Locate every uninfected red blood cell.
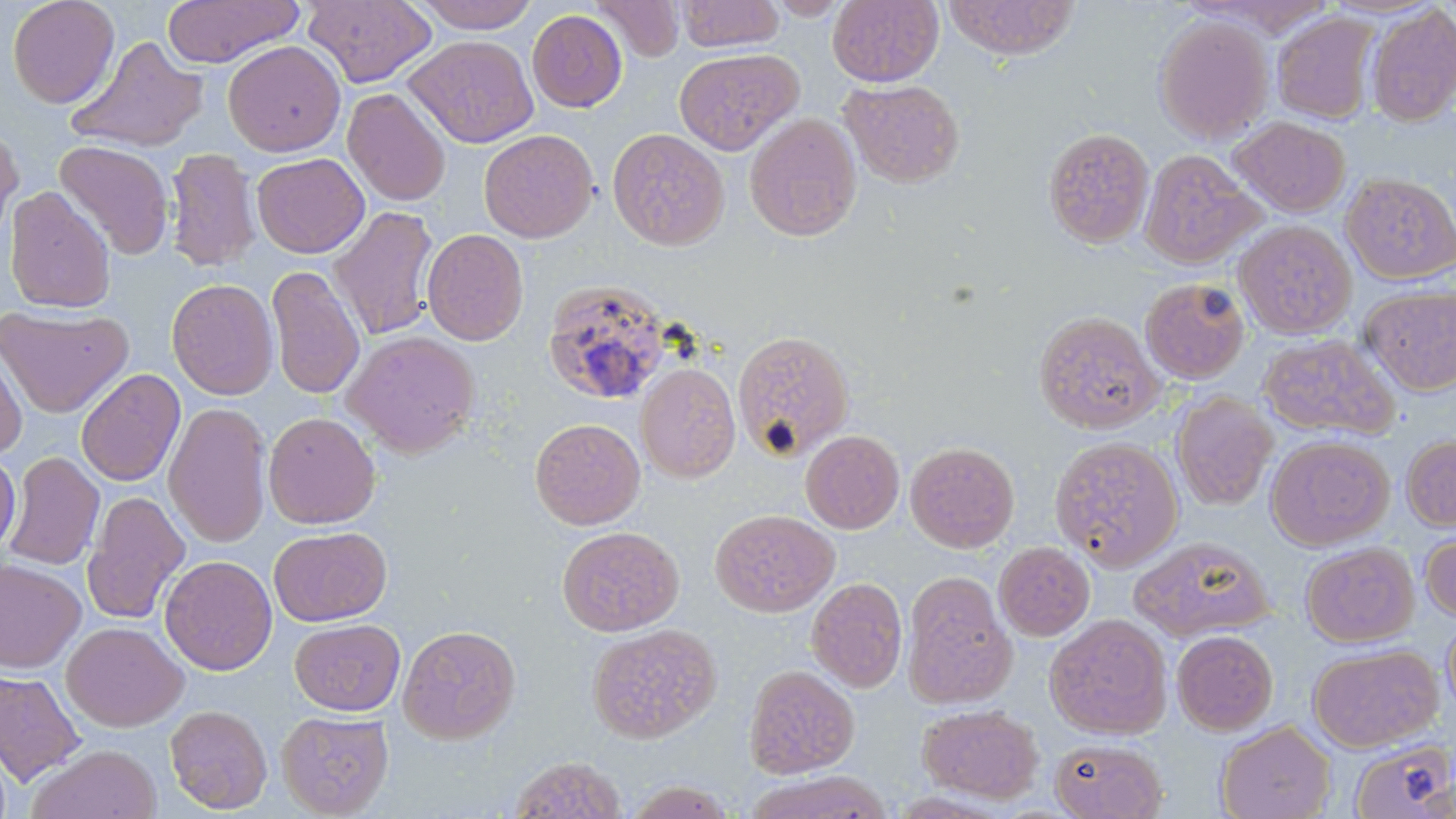

Approximate bounding boxes as [x1, y1, x2, y2] in pixels.
Uninfected red blood cells: [6, 0, 121, 109], [161, 0, 303, 67], [303, 0, 436, 86], [410, 0, 541, 33], [594, 0, 684, 60], [677, 0, 784, 51], [766, 0, 851, 20], [827, 0, 944, 87], [941, 0, 1079, 60], [1365, 6, 1456, 126], [527, 9, 627, 112], [1273, 11, 1380, 125], [1153, 13, 1273, 144], [68, 35, 209, 153], [404, 35, 539, 148], [223, 40, 346, 156], [674, 47, 802, 155], [839, 78, 965, 188], [343, 88, 451, 206], [744, 113, 863, 242], [1230, 116, 1351, 218], [0, 122, 24, 247], [607, 127, 729, 250], [1042, 127, 1154, 249], [479, 129, 599, 243], [54, 140, 174, 259], [164, 148, 261, 272], [1139, 148, 1263, 269], [251, 152, 370, 258], [1341, 172, 1456, 284], [3, 186, 117, 313], [328, 206, 441, 341], [1233, 219, 1357, 340], [422, 228, 529, 346], [266, 265, 366, 400], [1140, 277, 1251, 384], [166, 278, 279, 400], [541, 279, 671, 406], [1360, 283, 1456, 394], [0, 304, 134, 418], [1032, 309, 1164, 434], [733, 329, 855, 461], [343, 331, 480, 457], [1258, 332, 1399, 441], [0, 340, 28, 459], [636, 362, 741, 482], [76, 368, 185, 487], [1171, 391, 1278, 511], [164, 402, 273, 548], [263, 411, 381, 528], [530, 417, 646, 530], [800, 429, 905, 533], [1401, 433, 1456, 531], [1265, 434, 1395, 551], [1048, 435, 1184, 571], [905, 440, 1020, 553], [0, 451, 20, 557], [4, 452, 104, 571], [82, 490, 190, 625], [710, 508, 839, 617], [268, 525, 392, 626], [557, 525, 685, 636], [1420, 531, 1456, 622], [1130, 536, 1273, 641], [993, 541, 1095, 641], [1300, 541, 1419, 647], [159, 555, 277, 675], [0, 558, 86, 674], [902, 572, 1017, 709], [806, 576, 909, 693], [1045, 613, 1173, 740], [1442, 613, 1456, 722], [290, 618, 406, 715], [62, 622, 188, 732], [588, 623, 722, 743], [398, 624, 521, 744], [1171, 630, 1278, 735], [1308, 643, 1443, 752], [743, 664, 860, 778], [0, 668, 86, 787], [917, 703, 1044, 803], [164, 704, 273, 814], [276, 710, 395, 817], [1216, 721, 1335, 819], [1050, 738, 1168, 819], [1349, 738, 1455, 819], [26, 744, 162, 819], [509, 755, 627, 818], [744, 770, 892, 819], [623, 779, 739, 818].

slide-level diagnosis = Plasmodium ovale
image size = 1456×819 pixels
magnification = 1000x
modality = optical microscopy
stain = May-Grünwald-Giemsa
field of view = one of a larger specimen
preparation = thin blood smear